Assess the morphology of the red blood cells.
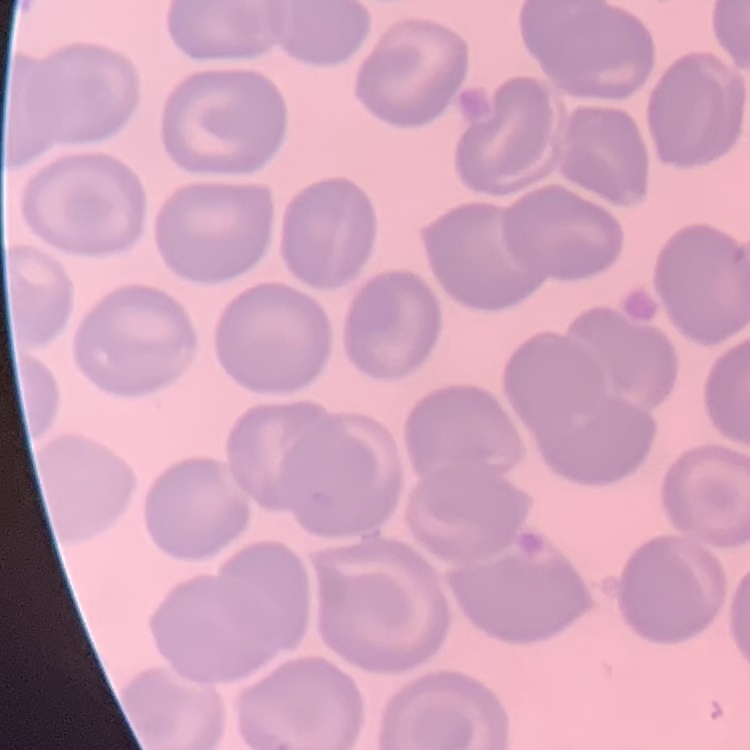

They show no rouleaux formation.

{
  "image_type": "one tile cut from a larger photomicrograph",
  "preparation": "thin blood smear",
  "stain": "Field's or Giemsa"
}